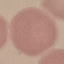

Result: no malaria parasites detected. Photographed with a smartphone camera at the microscope eyepiece. Giemsa-stained preparation. Thin blood smear. Automatically extracted cell patch, resized to 64 × 64 pixels.